Classify this cell by malaria status.
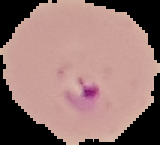
It is parasitized.

image type = segmented cell region on a black background
preparation = thin blood smear
image size = 160×145 pixels